Assess this cell for malaria.
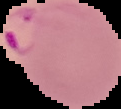

It is parasitized.

Cell region segmented out of the field of view; the surrounding area is masked to black. From a thin blood film. Image is 121×109 pixels.